Report the malaria status of this cell.
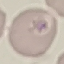
Uninfected.

{
  "preparation": "thin smear",
  "capture": "smartphone through the microscope eyepiece",
  "stain": "Giemsa",
  "image_type": "cell patch, automatically extracted from a larger field of view and resized to 64 × 64 pixels"
}